Give the extent of all uninfected red blood cells.
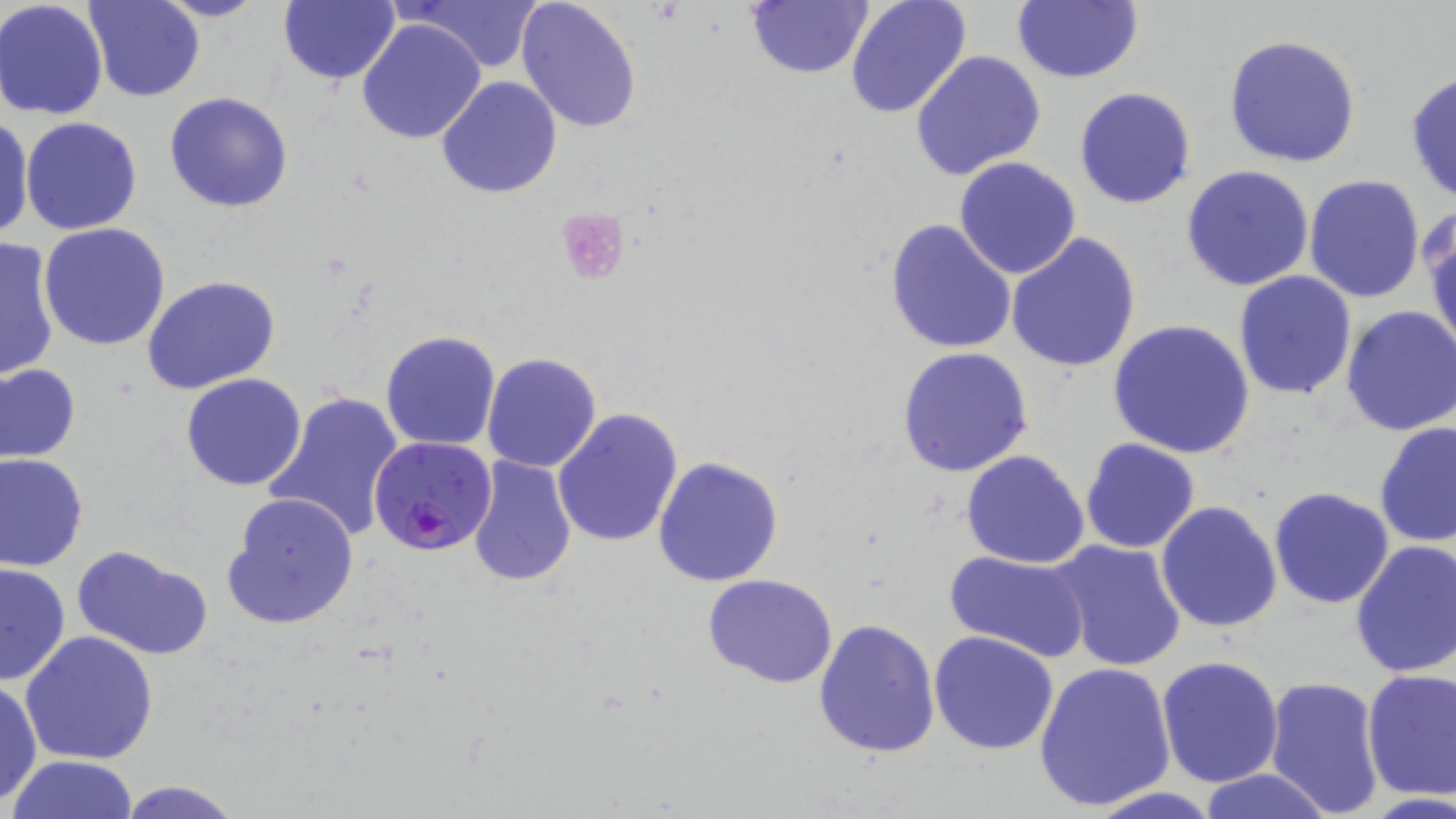
Approximate bounding boxes as (x1,y1)-(x2,y2) corner pairs in pixels.
Uninfected red blood cells: (0,0)-(108,120), (83,0)-(203,103), (152,0)-(267,23), (278,0)-(400,85), (402,0)-(544,72), (515,0)-(642,133), (843,0)-(971,121), (745,1)-(874,80), (1010,2)-(1144,85), (357,18)-(487,144), (1223,34)-(1362,168), (909,49)-(1046,181), (1405,69)-(1455,201), (437,76)-(563,199), (1074,87)-(1196,209), (164,91)-(294,212), (0,114)-(34,240), (21,117)-(143,236), (953,156)-(1083,280), (1181,165)-(1315,292), (1303,174)-(1428,303), (1424,211)-(1456,355), (885,217)-(1018,356), (39,223)-(171,352), (1006,231)-(1141,374), (0,234)-(59,382), (1233,270)-(1358,400), (142,274)-(281,393), (1340,306)-(1456,436), (1107,318)-(1256,458), (380,330)-(503,451), (896,345)-(1034,477), (481,353)-(602,474), (0,363)-(81,463), (181,373)-(307,491), (264,389)-(406,542), (552,407)-(684,547), (1374,420)-(1456,550), (1079,438)-(1201,553), (961,449)-(1090,569), (0,453)-(88,571), (463,456)-(577,590), (652,456)-(784,588), (1269,486)-(1396,608), (221,492)-(359,630), (1155,500)-(1284,633), (1048,540)-(1187,672), (1350,540)-(1456,679), (72,544)-(214,660), (943,548)-(1092,661), (0,561)-(71,685), (701,573)-(841,690), (814,618)-(941,759), (929,630)-(1058,754), (20,631)-(158,765), (1156,654)-(1285,788), (1032,663)-(1176,812), (1361,668)-(1456,802), (1262,674)-(1385,818), (0,680)-(43,808), (7,754)-(139,819), (1197,770)-(1331,819), (113,779)-(249,819).

Plasmodium falciparum-infected red blood cell locations: (368,435)-(497,558). Platelet locations: (553,207)-(630,288). Slide-level diagnosis: Plasmodium falciparum. Optical microscopy. One field of a larger specimen. Image is 1456×819 pixels. 1000x magnification. May-Grünwald-Giemsa-stained preparation. Thin blood film.